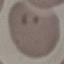

{
  "malaria_status": "parasitized",
  "capture": "smartphone through the microscope eyepiece",
  "preparation": "thin blood smear",
  "stain": "Giemsa",
  "image_type": "cell patch, automatically extracted from a larger field of view and resized to 64 × 64 pixels"
}